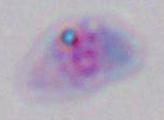
modality = photomicrograph
magnification = 1000x
identification = Toxoplasma gondii